State the blood parasite species.
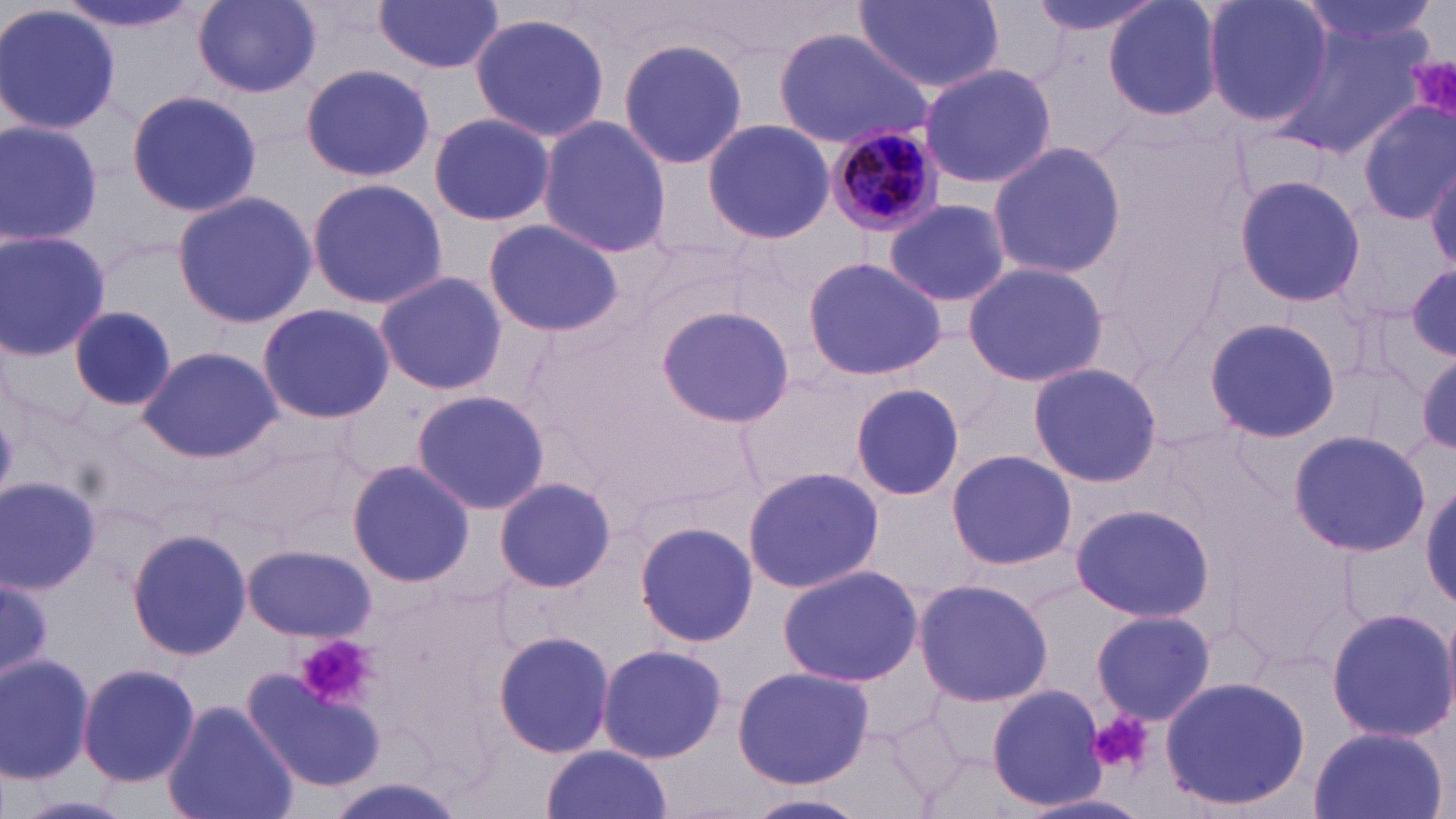

Plasmodium malariae.

preparation = thin blood film
uninfected red blood cell locations = approximate bounding boxes as (x1, y1, x2, y2) in pixels: (53, 0, 203, 36), (192, 0, 322, 96), (374, 0, 505, 75), (855, 0, 1005, 92), (1022, 0, 1173, 42), (1101, 0, 1226, 124), (1200, 0, 1334, 129), (1295, 0, 1436, 60), (0, 3, 121, 137), (468, 12, 611, 141), (1281, 15, 1433, 157), (772, 27, 932, 150), (618, 36, 751, 174), (918, 62, 1058, 191), (300, 63, 437, 184), (124, 88, 262, 215), (1357, 101, 1456, 225), (426, 113, 557, 226), (536, 116, 672, 257), (0, 119, 103, 245), (703, 119, 836, 244), (986, 139, 1127, 280), (1427, 158, 1456, 271), (1232, 174, 1363, 305), (305, 177, 447, 311), (172, 191, 318, 327), (884, 198, 1011, 308), (481, 218, 625, 338), (0, 231, 111, 358), (803, 257, 947, 381), (961, 261, 1108, 388), (1402, 265, 1456, 369), (373, 272, 508, 395), (257, 302, 396, 425), (70, 304, 176, 414), (655, 306, 795, 428), (1204, 315, 1343, 444), (137, 346, 280, 463), (1027, 362, 1164, 487), (850, 382, 964, 502), (411, 390, 552, 516), (1288, 431, 1428, 556), (946, 448, 1076, 570), (346, 460, 474, 587), (741, 465, 884, 595), (0, 476, 101, 592), (492, 477, 617, 593), (1422, 477, 1456, 612), (1068, 504, 1215, 623), (634, 521, 759, 648), (127, 528, 252, 661), (242, 544, 375, 640), (774, 564, 924, 686), (0, 576, 54, 682), (914, 578, 1054, 708), (1325, 606, 1456, 742), (1091, 609, 1216, 724), (493, 630, 618, 757), (597, 642, 728, 762), (0, 652, 97, 784), (77, 662, 200, 787), (732, 665, 877, 788), (249, 670, 386, 791), (1160, 674, 1312, 814), (986, 684, 1105, 809), (162, 700, 299, 819), (1308, 726, 1447, 819), (540, 744, 674, 819), (743, 791, 874, 819), (1015, 792, 1155, 819), (14, 794, 132, 818)
magnification = 1000x
stain = May-Grünwald-Giemsa
Plasmodium malariae-infected red blood cell locations = approximate bounding boxes as (x1, y1, x2, y2) in pixels: (825, 120, 950, 242)
modality = light microscopy
field of view = one of a larger specimen
image size = 1456×819 pixels
platelet locations = approximate bounding boxes as (x1, y1, x2, y2) in pixels: (1405, 56, 1456, 132), (296, 635, 376, 708), (1091, 711, 1153, 775)